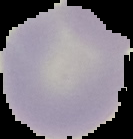

preparation: thin blood smear
malaria_status: uninfected
image_type: cell region segmented out of the field of view; surrounding area masked to black
image_size: 133×139 pixels